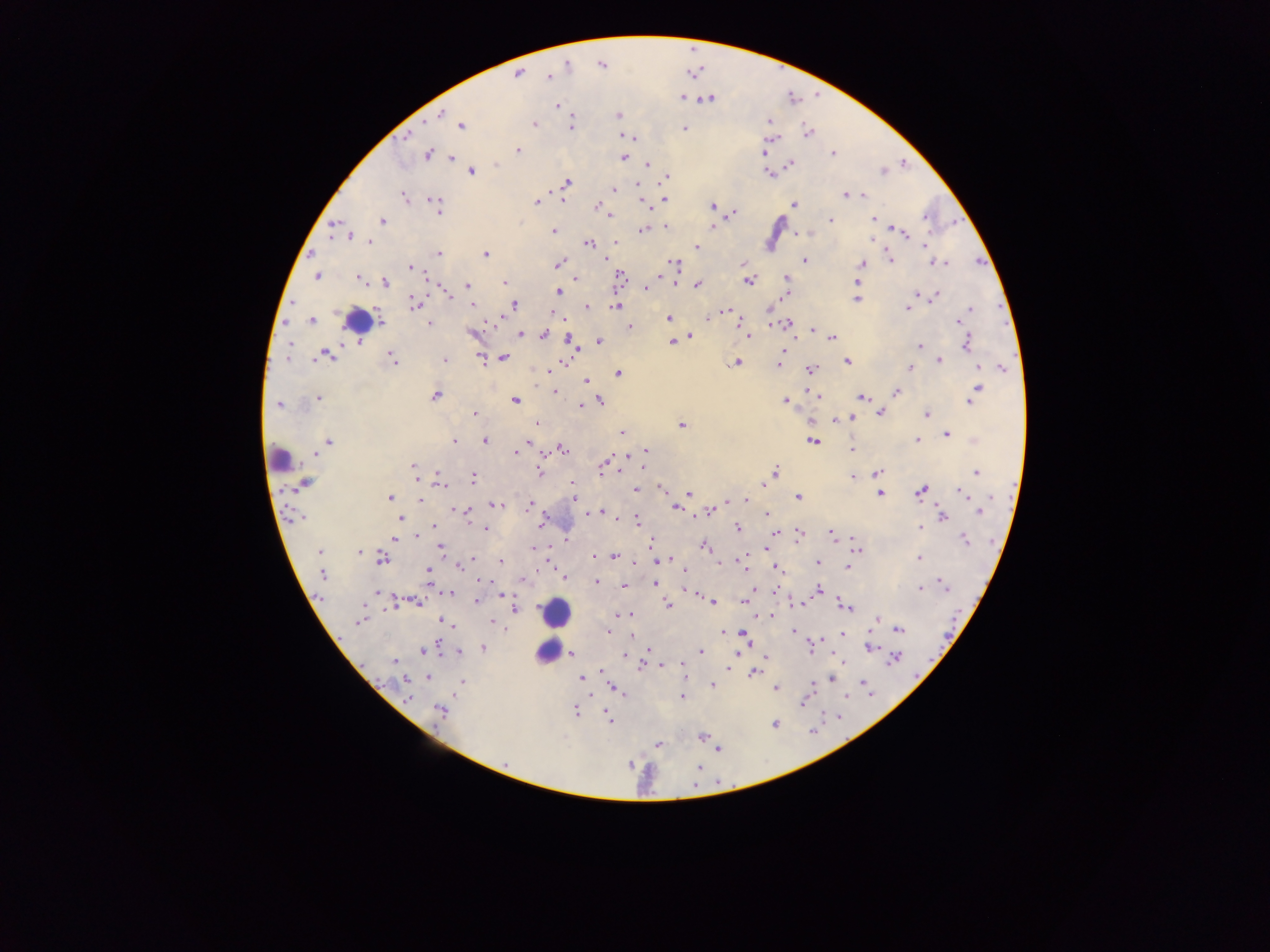

country = Ghana
malaria parasite locations = approximate centers as [x, y] in pixels: [568, 64], [601, 65], [518, 73], [549, 76], [682, 97], [709, 98], [557, 106], [441, 114], [617, 116], [768, 120], [534, 124], [460, 125], [570, 127], [685, 128], [808, 133], [628, 136], [405, 137], [773, 138], [518, 150], [764, 153], [832, 153], [428, 155], [622, 157], [451, 158], [902, 163], [495, 164], [648, 164], [790, 164], [470, 171], [882, 171], [768, 173], [666, 177], [566, 182], [637, 186], [614, 189], [846, 195], [863, 195], [405, 198], [665, 200], [535, 201], [794, 204], [597, 205], [437, 206], [711, 206], [732, 213], [607, 214], [925, 218], [830, 219], [873, 219], [382, 220], [333, 226], [665, 226], [711, 227], [896, 228], [642, 230], [552, 231], [900, 231], [809, 233], [796, 234], [350, 235], [869, 238], [369, 242], [615, 242], [589, 243], [925, 246], [696, 247], [438, 253], [485, 254], [889, 258], [804, 259], [675, 263], [933, 263], [944, 263], [558, 264], [861, 264], [741, 265], [409, 266], [317, 275], [661, 275], [620, 276], [360, 278], [786, 278], [575, 279], [748, 280], [505, 282], [677, 282], [855, 282], [384, 283], [697, 284], [467, 285], [646, 287], [561, 289], [558, 291], [447, 296], [934, 297], [855, 298], [414, 303], [512, 304], [910, 304], [472, 305], [616, 305], [585, 306], [907, 308], [970, 309], [724, 311], [552, 315], [668, 318], [708, 318], [957, 319], [312, 320], [491, 320], [962, 321], [380, 322], [789, 323], [429, 324], [770, 324], [741, 325], [629, 327], [811, 329], [472, 333], [525, 333], [519, 334], [543, 334], [566, 334], [749, 336], [689, 337], [792, 338], [832, 338], [569, 339], [599, 341], [671, 341], [966, 343], [288, 345], [919, 347], [575, 351], [783, 351], [326, 355], [392, 357], [481, 357], [503, 358], [780, 359], [444, 360], [938, 360], [845, 361], [737, 362], [778, 364], [552, 366], [978, 367], [1001, 367], [809, 368], [910, 368], [550, 370], [617, 374], [584, 381], [977, 388], [553, 391], [896, 392], [808, 393], [435, 396], [818, 396], [862, 396], [318, 397], [514, 400], [599, 401], [786, 401], [970, 401], [278, 404], [581, 406], [879, 412], [474, 413], [926, 415], [852, 416], [812, 419], [836, 419], [537, 424], [681, 424], [621, 432], [947, 433], [484, 440], [813, 440], [916, 440], [974, 440], [329, 441], [454, 441], [851, 448], [562, 449], [647, 450], [516, 452], [315, 454], [628, 455], [607, 462], [644, 465], [414, 466], [601, 467], [539, 472], [775, 472], [975, 472], [877, 473], [417, 477], [472, 477], [853, 477], [303, 483], [573, 483], [439, 484], [763, 486], [572, 489], [636, 489], [660, 489], [921, 491], [960, 491], [687, 493], [879, 493], [988, 495], [797, 496], [390, 497], [573, 497], [420, 500], [745, 500], [730, 501], [726, 503], [496, 504], [529, 505], [674, 508], [454, 510], [711, 511], [465, 512], [599, 512], [979, 512], [585, 513], [766, 514], [942, 516], [301, 517], [615, 517], [400, 519], [636, 521], [541, 522], [433, 526], [486, 528], [736, 528], [919, 528], [830, 530], [774, 534], [415, 535], [797, 536], [831, 536], [854, 538], [394, 539], [963, 539], [651, 542], [441, 546], [705, 546], [533, 549], [764, 550], [857, 550], [319, 551], [359, 552], [592, 556], [614, 556], [381, 559], [471, 559], [670, 559], [740, 559], [919, 559], [500, 561], [655, 561], [662, 561], [817, 562], [743, 563], [718, 564], [457, 565], [846, 567], [774, 568], [427, 569], [684, 570], [322, 574], [565, 577], [522, 580], [485, 581], [597, 582], [654, 583], [624, 585], [489, 586], [944, 587], [918, 588], [818, 589], [688, 590], [773, 590], [376, 593], [451, 593], [503, 595], [742, 599], [476, 600], [712, 601], [416, 602], [392, 603], [841, 603], [667, 604], [792, 604], [846, 605], [514, 609], [616, 614], [630, 614], [770, 615], [759, 617], [876, 618], [359, 620], [444, 621], [491, 622], [450, 623], [454, 624], [505, 629], [897, 629], [608, 630], [793, 630], [723, 632], [743, 633], [842, 634], [820, 639], [746, 641], [482, 647], [869, 647], [430, 648], [648, 648], [810, 648], [423, 650], [701, 651], [457, 653], [737, 653], [571, 654], [624, 656], [766, 656], [896, 657], [842, 660], [394, 662], [663, 665], [639, 666], [601, 669], [727, 669], [754, 672], [685, 674], [428, 677], [581, 678], [830, 678], [406, 681], [461, 681], [862, 682], [711, 685], [775, 687], [616, 689], [866, 691], [844, 695], [591, 696], [681, 696], [407, 697], [803, 700], [440, 711], [575, 713], [607, 716], [774, 724], [701, 736], [658, 745], [719, 749], [504, 763], [630, 764]
image size = 1270×952 pixels
capture = mobile-phone photograph through a microscope
leukocyte locations = approximate centers as [x, y] in pixels: [357, 320], [280, 460], [555, 613], [546, 650]
field of view = single
preparation = thick blood film